Classify this cell by malaria status.
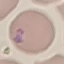

Parasitized.

Summary:
  - Capture: smartphone through the microscope eyepiece
  - Image type: cell patch, automatically extracted from a larger field of view and resized to 64 × 64 pixels
  - Preparation: thin blood film
  - Stain: Giemsa